Name the cell type shown.
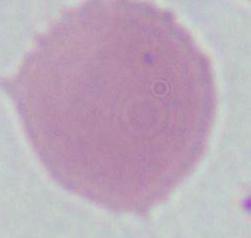
This is an erythrocyte.

Summary:
  - Modality: micrograph
  - Magnification: 1000x